Assess the morphology of the red blood cells.
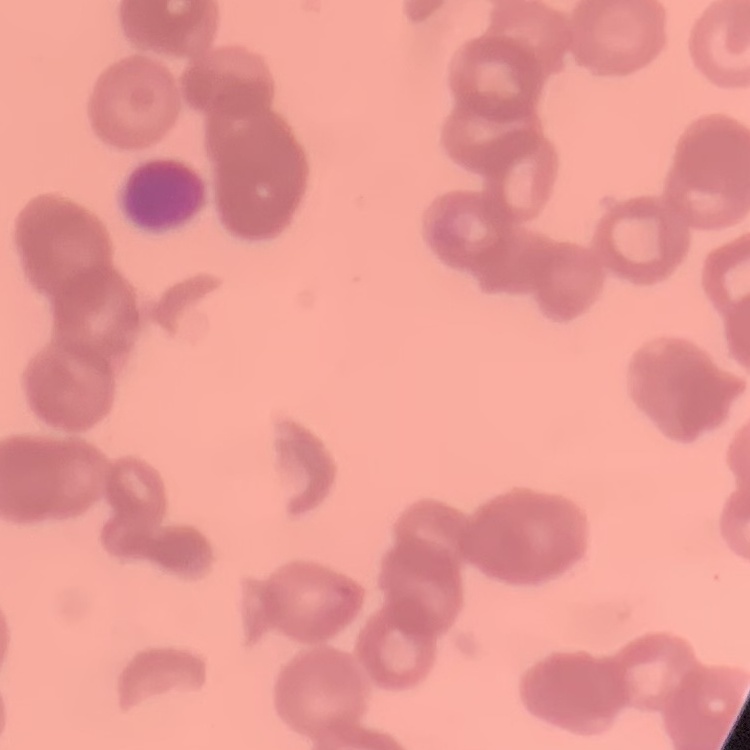

Rouleaux formation.

Summary:
  - Image type: square crop of a larger photomicrograph
  - Stain: Field's or Giemsa
  - Preparation: thin blood film